Comment on the morphology of the red blood cells.
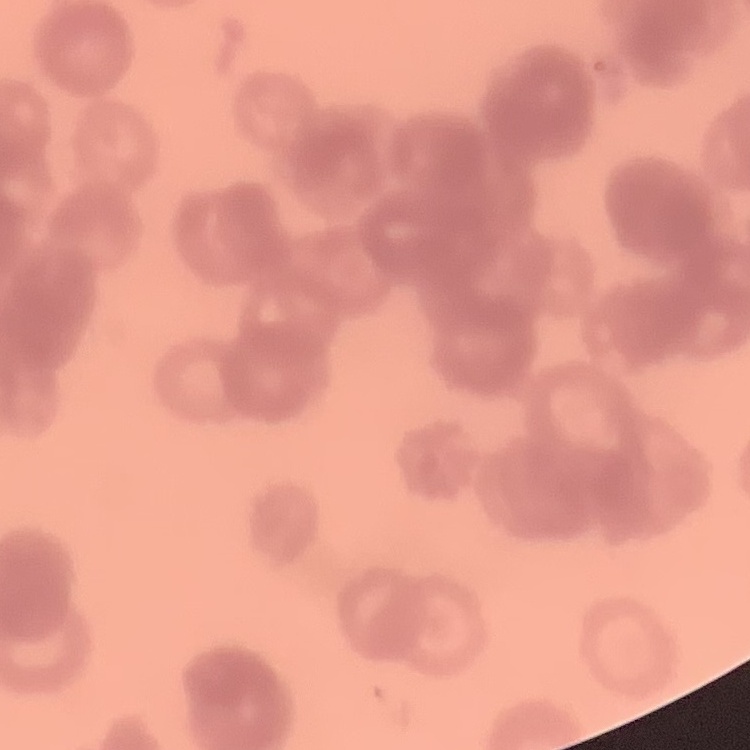
Rouleaux formation.

Thin blood film. One tile cut from a larger photomicrograph. Field's or Giemsa stain.